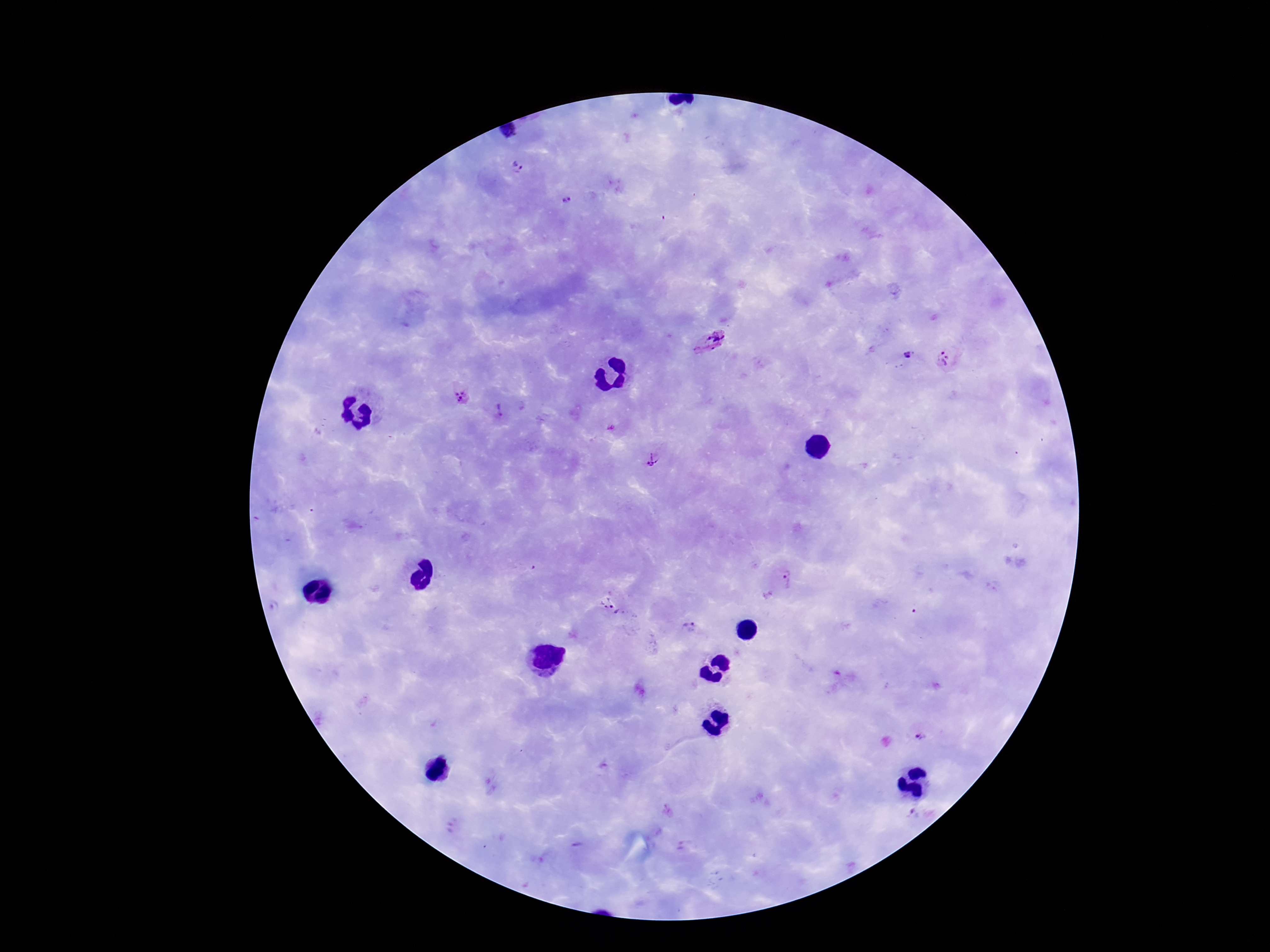

preparation = thick blood film
image size = 1270×952 pixels
patient malaria status = positive
field of view = one from this slide
Plasmodium parasite locations = approximate centers as {x, y} in pixels: {518, 168}, {566, 201}, {709, 343}, {907, 357}, {945, 361}, {462, 397}, {501, 411}, {654, 460}, {787, 578}, {610, 606}, {274, 607}, {689, 626}, {920, 740}, {667, 812}, {912, 815}
magnification = 100x
capture = smartphone camera through the microscope eyepiece
stain = Giemsa